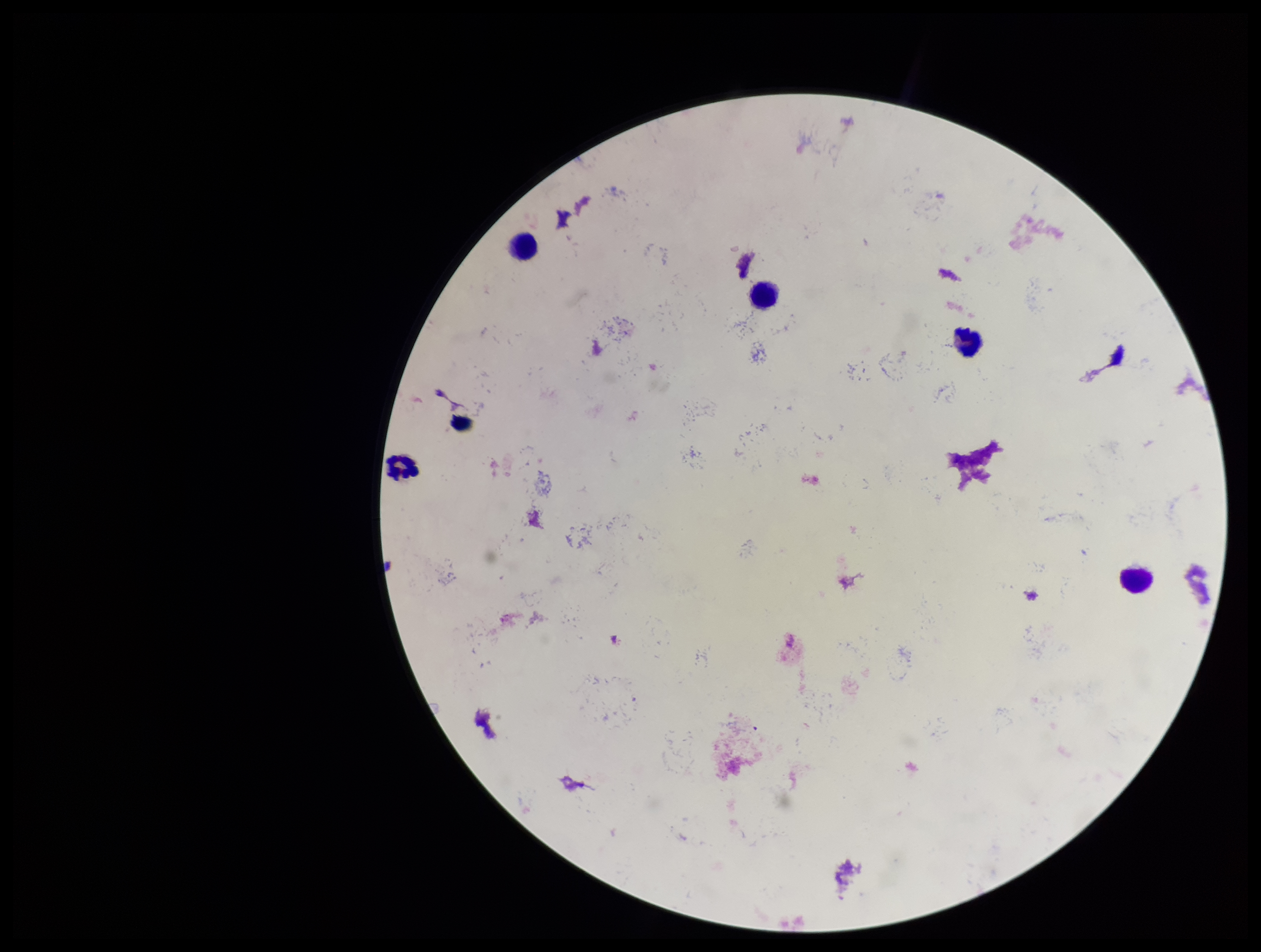

Parasite count: 0. Image is 1261×952 pixels. Patient malaria status: negative. One field from this slide. Preparation: thick blood smear. Photographed through the microscope eyepiece with a smartphone camera. Giemsa stain. Leukocyte count: 5. Plasmodium parasites: none identified.